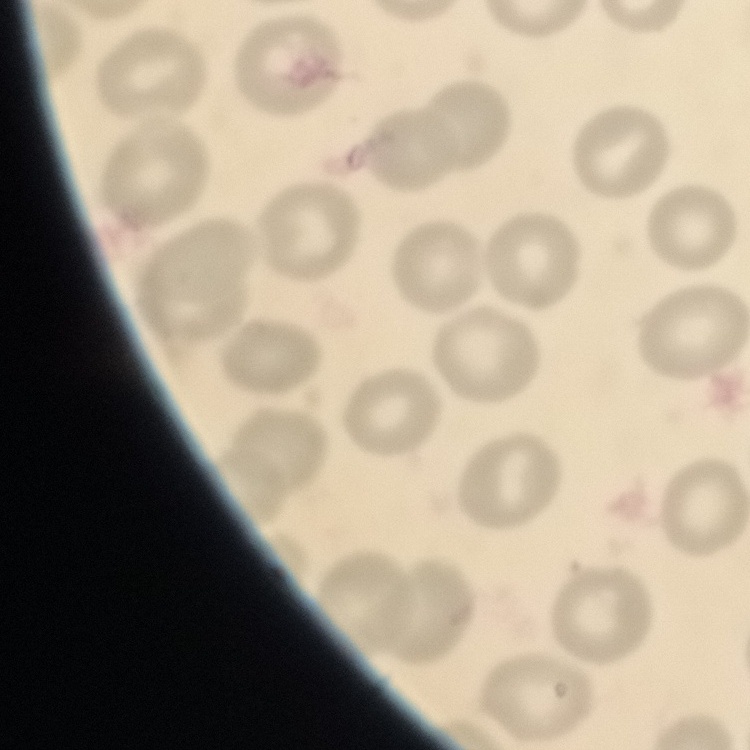
The erythrocytes exhibit no rouleaux formation. Thin peripheral smear. Field's or Giemsa stain. One tile cut from a larger photomicrograph.